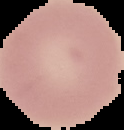
{
  "image_size": "124×130 pixels",
  "image_type": "segmented cell region on a black background",
  "malaria_status": "uninfected",
  "preparation": "thin blood smear"
}